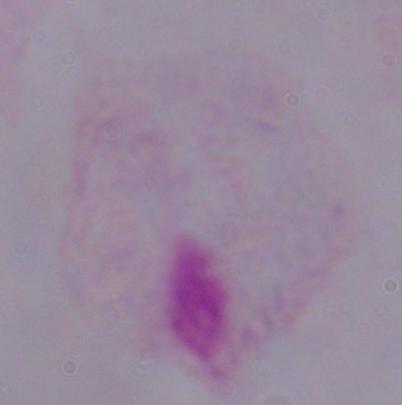
{
  "modality": "micrograph",
  "identification": "trichomonad",
  "magnification": "1000x"
}